Give the preparation type.
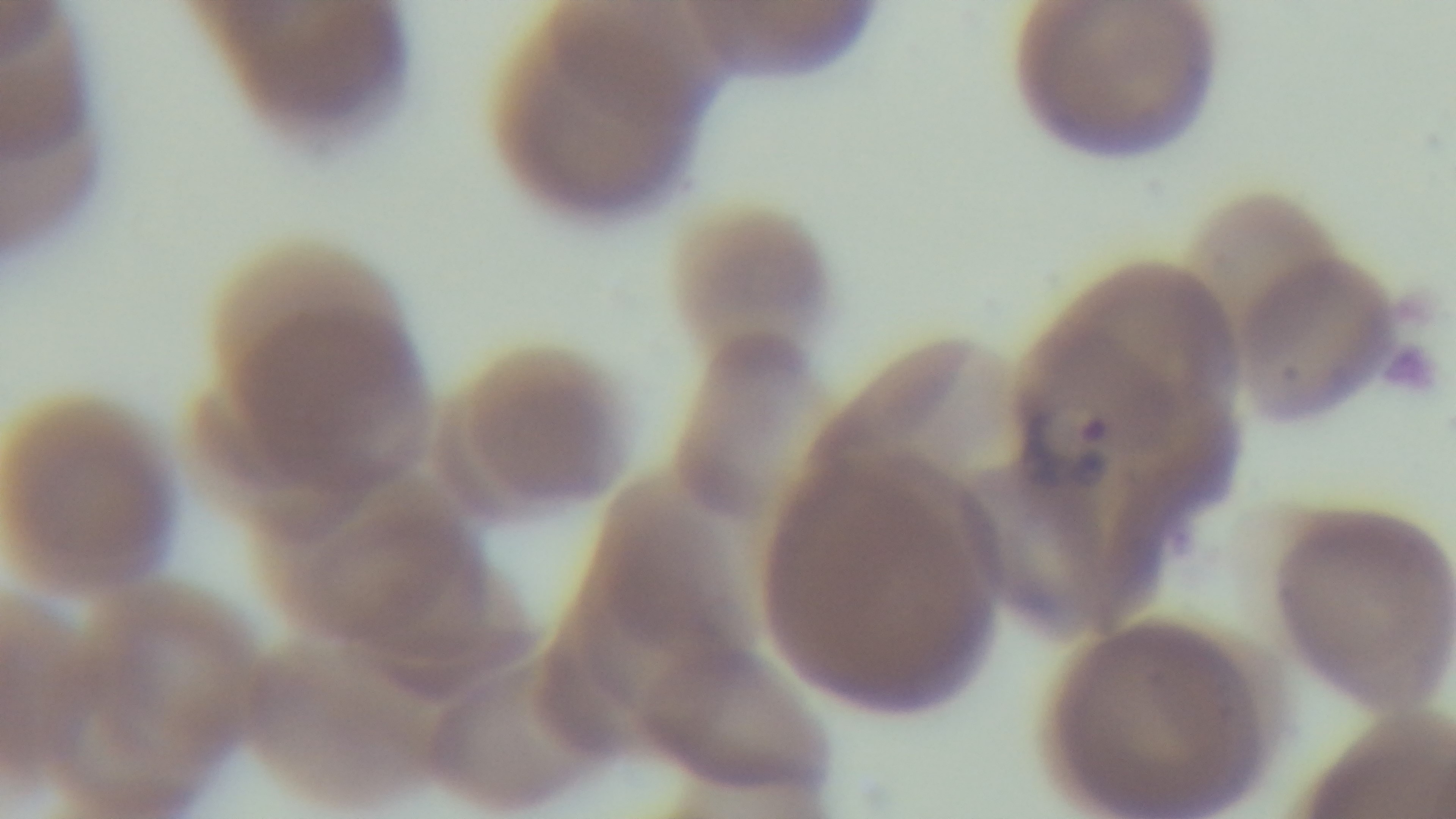
It is a thin blood film.

100x oil-immersion objective. Giemsa stain. One field from the slide. Mounted 4K digital camera. Malaria status: infected. Light microscopy.